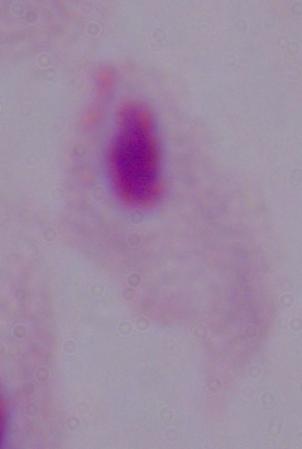
modality = micrograph
magnification = 1000x
identification = trichomonad